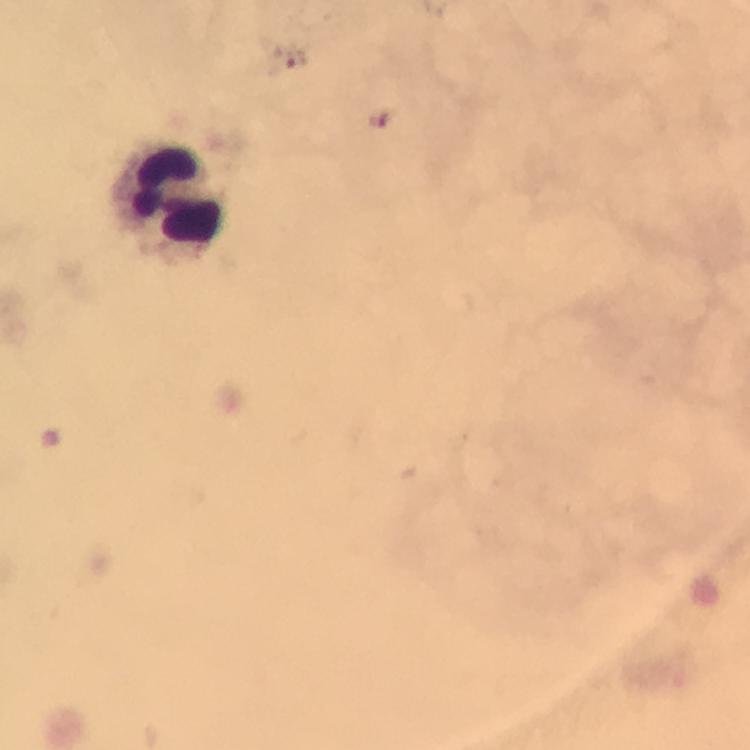

Approximate object centers, in pixels from the top-left corner.
Summary:
  - Leukocyte locations: (x=169, y=195)
  - Immersion oil: used
  - Magnification: 100x
  - Cropped from: a single field of view
  - Plasmodium parasites: none detected
  - Capture: smartphone camera through the microscope
  - Context: from a malaria diagnostic workup
  - Preparation: thick blood film
  - Stain: Giemsa
  - Image size: 750×750 pixels